State the preparation type.
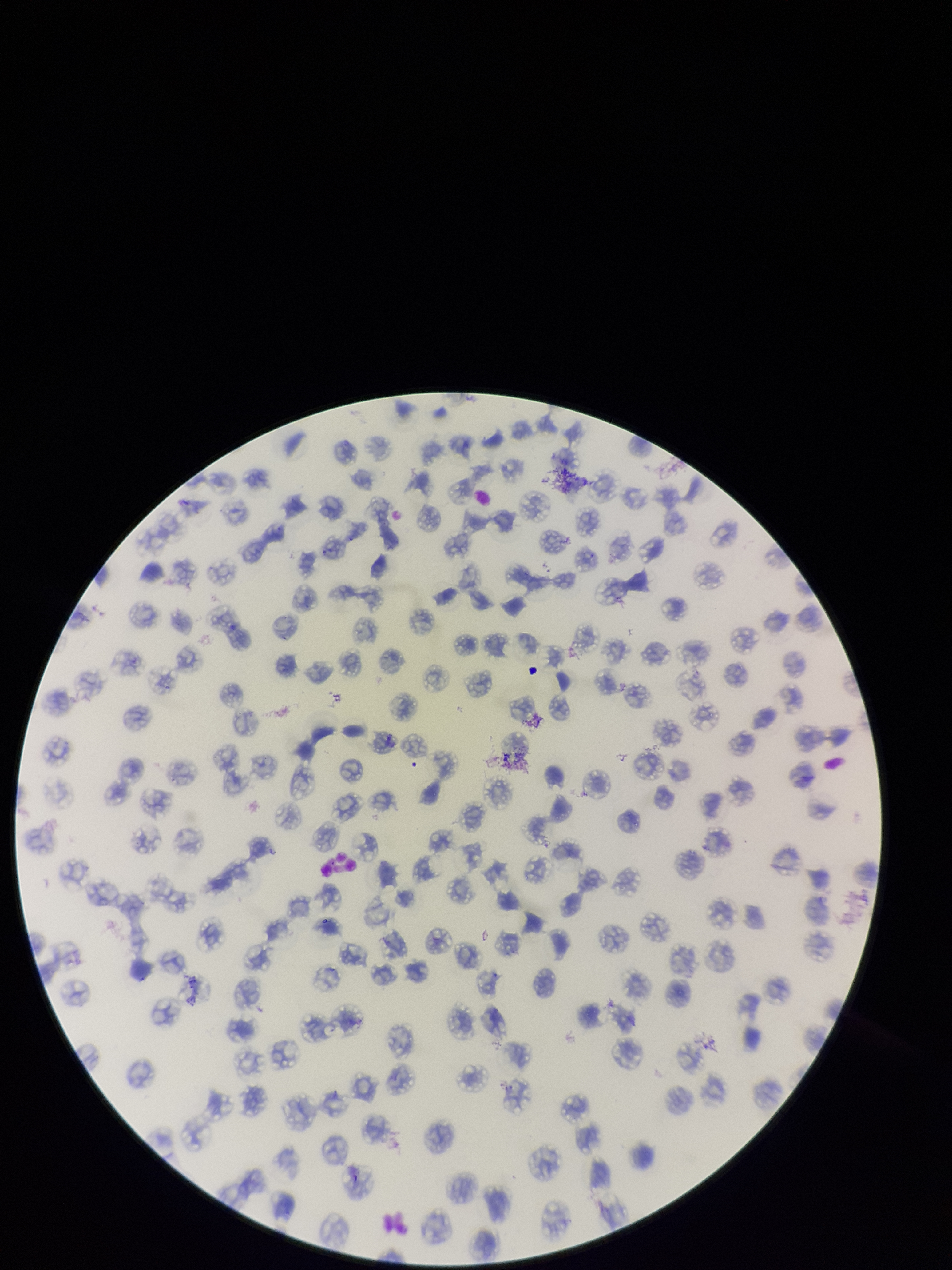
A thin smear.

Patient malaria status: positive. Giemsa stain. One field from this slide. Smartphone photograph taken through the eyepiece of a microscope. Parasitized red blood cell count: 0. Red blood cell count: 177. Image is 952×1270 pixels. Parasitized red blood cells: none detected. Species reported for this patient: Plasmodium falciparum.